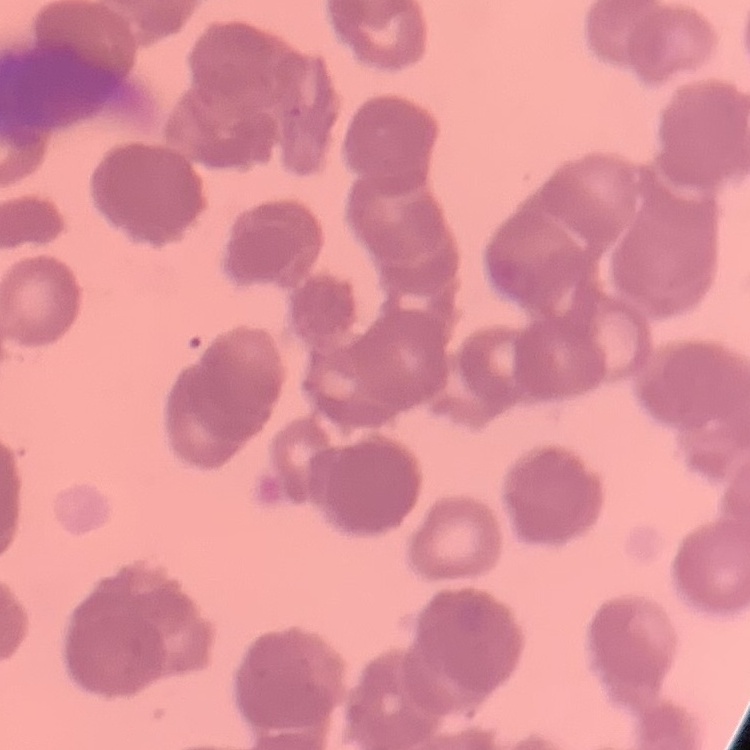

The red blood cells show rouleaux formation. One tile cut from a larger photomicrograph. Stained with either Field's or Giemsa. Thin peripheral smear.